Locate and identify every blood parasite.
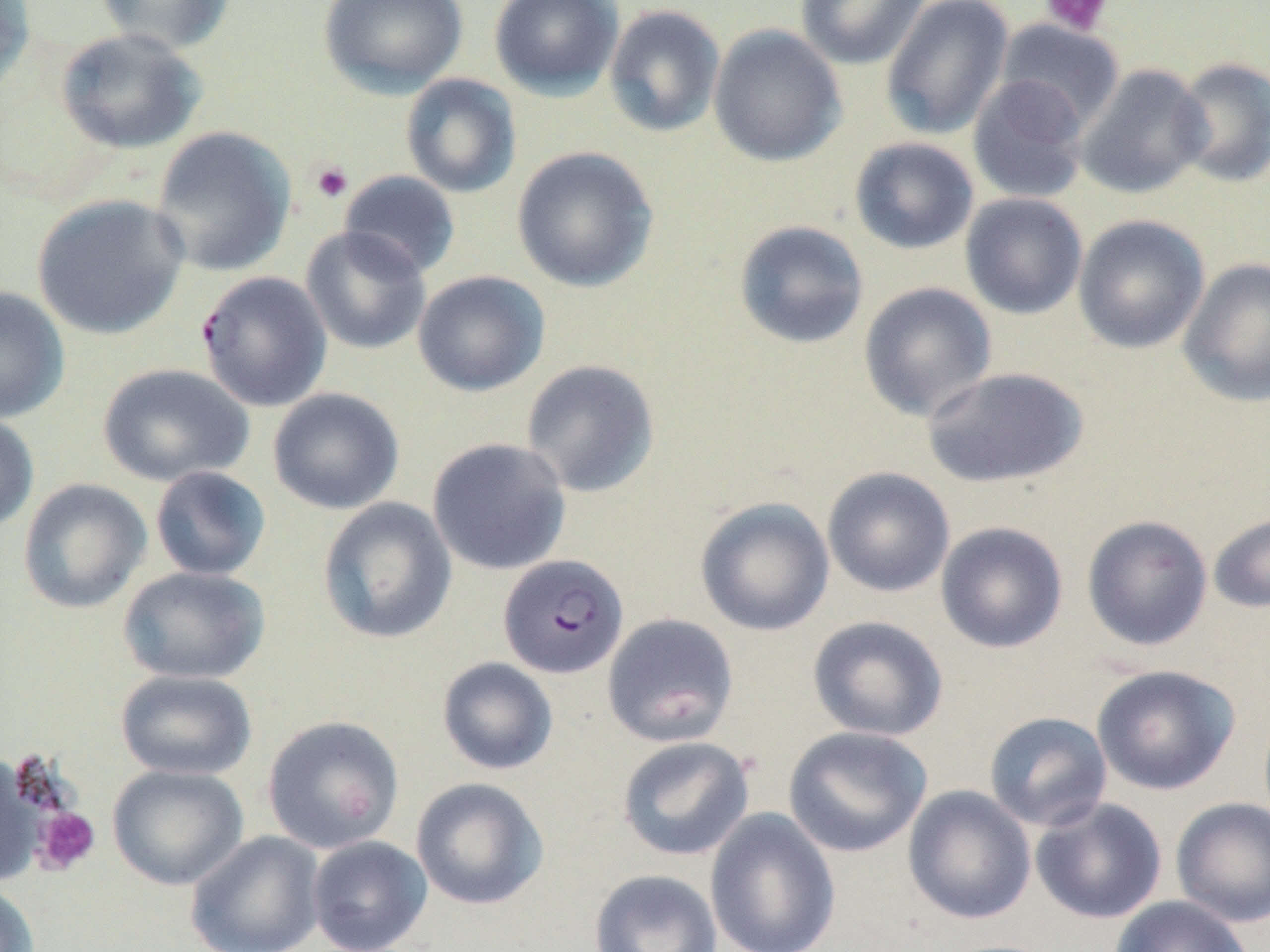
Approximate bounding boxes as (x1, y1, x2, y2) in pixels.
Plasmodium falciparum-infected red blood cells: (195, 270, 333, 412), (498, 554, 629, 679).
No Plasmodium ovale, Plasmodium malariae, Plasmodium vivax, Babesia divergens, or Trypanosoma brucei observed.

Uninfected red blood cell locations: (0, 0, 36, 96), (93, 0, 238, 55), (318, 0, 468, 97), (489, 0, 623, 99), (794, 0, 930, 70), (880, 0, 1014, 141), (604, 4, 726, 138), (994, 18, 1125, 133), (707, 24, 847, 167), (55, 27, 206, 154), (1171, 56, 1270, 188), (1075, 63, 1212, 199), (400, 73, 521, 199), (967, 74, 1091, 205), (149, 126, 297, 277), (849, 137, 980, 255), (510, 146, 659, 293), (339, 170, 461, 279), (960, 192, 1088, 320), (31, 193, 190, 340), (1072, 214, 1210, 354), (733, 220, 869, 350), (299, 226, 432, 355), (1178, 257, 1270, 408), (412, 270, 550, 397), (857, 281, 997, 422), (0, 286, 70, 423), (520, 359, 661, 498), (97, 362, 254, 488), (920, 366, 1089, 489), (268, 387, 405, 515), (0, 412, 40, 534), (427, 437, 571, 576), (149, 466, 271, 582), (822, 467, 955, 597), (18, 478, 152, 614), (317, 497, 458, 645), (695, 497, 835, 636), (1207, 511, 1270, 614), (1081, 515, 1213, 651), (935, 521, 1068, 654), (118, 566, 270, 685), (602, 613, 739, 747), (807, 615, 948, 741), (437, 657, 559, 775), (1091, 664, 1240, 795), (115, 669, 257, 781), (984, 711, 1113, 832), (262, 715, 405, 854), (783, 725, 932, 857), (616, 735, 755, 861), (0, 755, 47, 887), (107, 764, 249, 890), (410, 777, 549, 911), (902, 784, 1036, 925), (1170, 796, 1270, 928), (1031, 797, 1167, 924), (704, 808, 841, 952), (185, 831, 326, 952), (306, 835, 432, 952), (588, 869, 723, 952), (0, 882, 40, 952), (1109, 895, 1254, 952). Platelet locations: (1040, 0, 1113, 37), (309, 160, 354, 204), (33, 806, 101, 874). Slide-level diagnosis: Plasmodium falciparum. May-Grünwald-Giemsa stain. Captured at 1000x magnification. Light microscopy. Image is 1270×952 pixels. Single field of view. Thin blood smear.